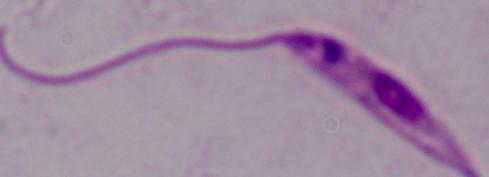
Photomicrograph. 1000x magnification. A Leishmania parasite is seen.